Identify the blood parasite species.
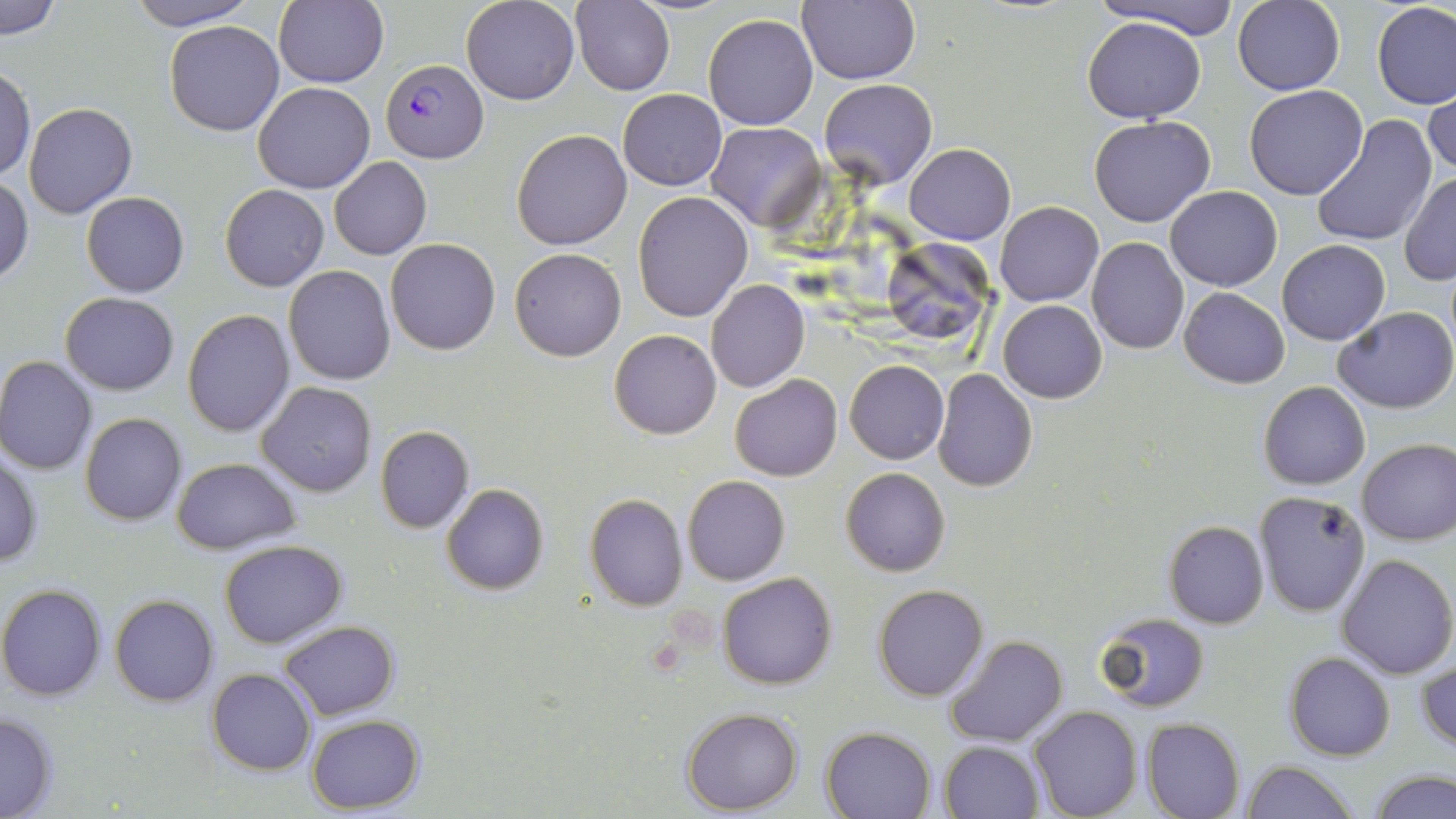

Plasmodium falciparum.

uninfected red blood cell locations = approximate bounding boxes as (x1,y1)-(x2,y2) corner pairs in pixels: (126,0)-(259,30), (275,0)-(389,89), (461,0)-(579,104), (1093,0)-(1243,37), (0,1)-(62,37), (573,1)-(673,96), (796,1)-(920,86), (1232,1)-(1344,95), (1371,1)-(1456,109), (702,14)-(818,130), (1083,16)-(1204,123), (166,21)-(285,135), (0,67)-(35,180), (820,79)-(937,189), (1424,80)-(1456,182), (253,81)-(376,194), (1244,84)-(1369,199), (618,89)-(727,191), (24,103)-(138,219), (1089,115)-(1215,227), (1311,115)-(1437,247), (707,122)-(826,230), (512,129)-(633,250), (906,144)-(1015,245), (329,156)-(432,260), (1400,173)-(1456,284), (0,176)-(33,285), (220,185)-(329,292), (1165,185)-(1283,292), (632,190)-(753,322), (80,191)-(189,297), (996,201)-(1103,306), (1086,238)-(1189,354), (386,239)-(501,354), (881,239)-(990,346), (1277,240)-(1390,345), (510,248)-(626,360), (283,264)-(396,385), (706,279)-(809,393), (1178,287)-(1290,387), (59,292)-(179,394), (998,300)-(1107,402), (1333,307)-(1456,414), (182,309)-(295,436), (608,328)-(722,440), (0,355)-(97,474), (845,360)-(948,464), (932,368)-(1038,492), (730,373)-(842,481), (257,381)-(377,496), (1258,381)-(1369,490), (80,412)-(187,526), (374,425)-(474,532), (1357,436)-(1456,545), (0,452)-(43,570), (171,457)-(301,554), (841,467)-(950,576), (682,475)-(789,586), (441,483)-(549,596), (1252,488)-(1371,616), (584,493)-(688,610), (1162,519)-(1268,628), (219,539)-(347,647), (1336,553)-(1455,677), (717,572)-(837,690), (0,583)-(109,701), (873,583)-(989,702), (110,594)-(219,706), (1095,611)-(1209,713), (278,619)-(399,720), (946,636)-(1066,746), (1285,652)-(1395,761), (1417,659)-(1456,754), (208,667)-(315,775), (1028,705)-(1141,819), (0,708)-(59,818), (681,708)-(802,814), (305,714)-(426,814), (1142,717)-(1244,819), (822,726)-(935,818), (938,740)-(1045,819), (1241,760)-(1358,819), (1367,769)-(1456,819)
magnification = 1000x
preparation = thin blood film
field of view = one of a larger specimen
Plasmodium falciparum-infected red blood cell locations = approximate bounding boxes as (x1,y1)-(x2,y2) corner pairs in pixels: (380,59)-(488,163)
image size = 1456×819 pixels
stain = May-Grünwald-Giemsa
modality = optical microscopy